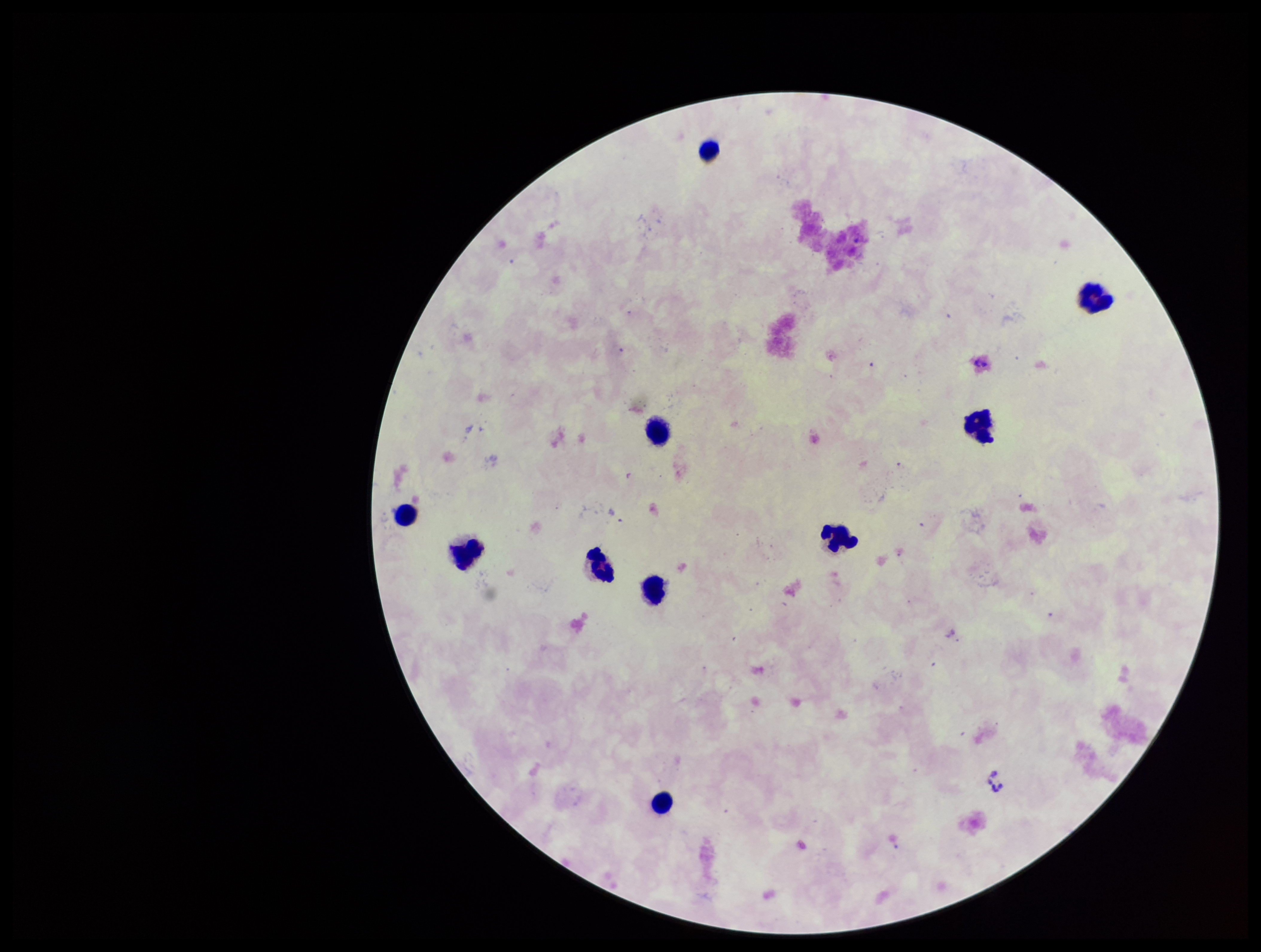

Summary:
  - Parasite count: 0
  - Field of view: one from this slide
  - Plasmodium parasites: none detected
  - Capture: smartphone photograph through the microscope eyepiece
  - Leukocyte count: 10
  - Preparation: thick smear
  - Stain: Giemsa
  - Image size: 1261×952 pixels
  - Patient malaria status: negative